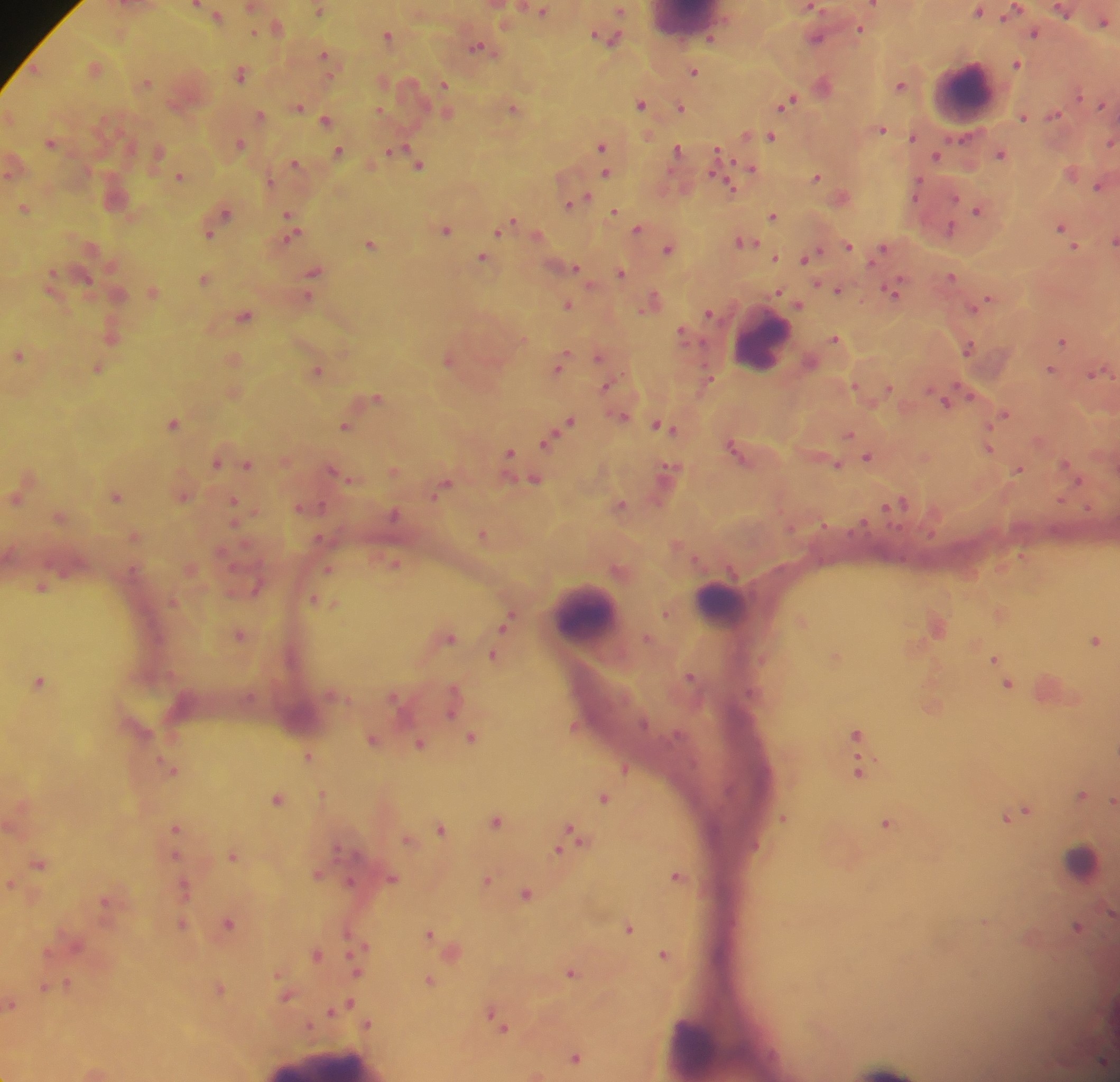
Approximate centers as (x, y) in pixels. Leukocyte locations: (964, 92), (763, 342), (722, 602), (587, 611), (1082, 860), (695, 1050). Plasmodium parasite locations: (196, 3), (874, 3), (812, 6), (1015, 8), (319, 9), (543, 9), (620, 10), (978, 10), (1064, 11), (218, 14), (1104, 20), (860, 28), (254, 31), (1035, 32), (388, 35), (607, 36), (711, 37), (817, 37), (477, 46), (324, 54), (1017, 63), (694, 70), (240, 73), (147, 81), (444, 83), (900, 84), (1079, 94), (787, 101), (640, 103), (1101, 104), (299, 106), (681, 106), (513, 107), (379, 109), (259, 113), (1054, 114), (1023, 116), (10, 117), (327, 120), (881, 129), (746, 134), (771, 135), (913, 136), (50, 142), (239, 142), (1111, 142), (601, 145), (397, 147), (677, 148), (338, 150), (159, 151), (390, 151), (717, 152), (1000, 153), (937, 155), (295, 162), (419, 164), (751, 168), (606, 172), (180, 175), (817, 176), (1098, 185), (730, 186), (917, 186), (586, 195), (575, 199), (568, 203), (25, 207), (977, 209), (615, 210), (225, 212), (288, 212), (773, 215), (512, 221), (290, 223), (506, 225), (1060, 226), (637, 227), (949, 228), (447, 229), (498, 231), (209, 234), (290, 236), (1114, 240), (745, 241), (370, 243), (847, 244), (1074, 245), (882, 247), (668, 248), (775, 256), (482, 257), (806, 257), (575, 267), (314, 270), (621, 272), (53, 274), (951, 275), (87, 278), (204, 278), (837, 288), (894, 290), (779, 292), (308, 295), (987, 298), (649, 302), (567, 304), (800, 305), (975, 305), (708, 312), (244, 314), (681, 331), (835, 338), (1063, 340), (969, 347), (19, 355), (599, 356), (447, 360), (561, 363), (97, 368), (318, 370), (1050, 370), (1096, 372), (708, 375), (606, 386), (889, 387), (968, 392), (378, 395), (945, 400), (1004, 414), (623, 415), (570, 421), (174, 422), (345, 425), (662, 426), (849, 433), (546, 441), (988, 447), (735, 450), (509, 451), (867, 456), (216, 462), (248, 463), (838, 463), (1067, 465), (333, 469), (394, 469), (667, 469), (1020, 469), (350, 479), (535, 479), (1077, 480), (444, 484), (117, 496), (16, 498), (234, 500), (1059, 500), (899, 502), (621, 504), (322, 505), (302, 507), (1087, 508), (394, 514), (823, 522), (861, 522), (482, 533), (319, 537), (395, 563), (328, 568), (41, 587), (257, 588), (315, 599), (326, 602), (665, 613), (507, 622), (239, 634), (450, 636), (1095, 640), (493, 655), (994, 658), (690, 675), (40, 681), (1007, 683), (453, 690), (394, 696), (451, 712), (643, 723), (574, 726), (856, 732), (472, 736), (373, 738), (419, 743), (308, 755), (172, 768), (624, 768), (858, 770), (323, 794), (1082, 794), (604, 797), (278, 798), (1113, 799), (1025, 810), (1016, 814), (1006, 817), (783, 818), (495, 821), (886, 822), (175, 826), (441, 828), (570, 830), (407, 839), (566, 840), (558, 851), (174, 854), (233, 855), (39, 863), (317, 874), (677, 874), (393, 878), (487, 880), (351, 881), (10, 882), (184, 886), (526, 893), (104, 901), (1111, 913), (228, 923), (182, 924), (1077, 926), (629, 927), (429, 933), (358, 950), (315, 954), (664, 954), (358, 970), (571, 972), (430, 980), (67, 985), (45, 988), (219, 988), (286, 997), (349, 1003), (12, 1004), (341, 1007), (331, 1011), (492, 1017), (368, 1023), (502, 1026), (575, 1056). Image is 1120×1082 pixels. Single field of view. Collected in Ghana. Thick blood film. Photographed through a microscope with a mobile-phone camera.